Locate every blood parasite and identify its species.
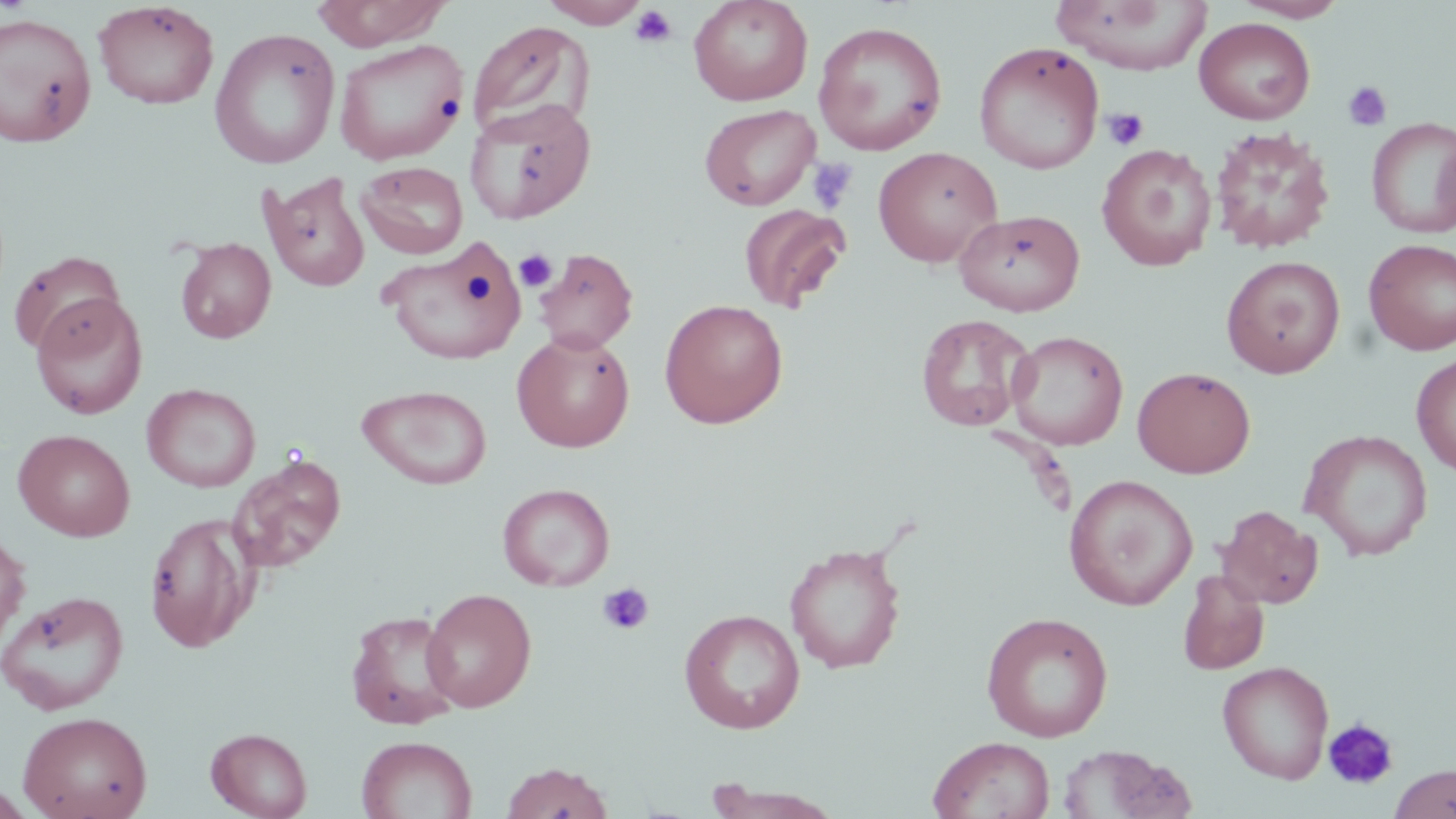
No blood parasites seen.

{
  "slide_level_diagnosis": "no evidence of blood parasites",
  "uninfected_red_blood_cell_locations": "approximate bounding boxes as named x1/y1/x2/y2 corners in pixels: (x1=311, y1=0, x2=452, y2=50), (x1=538, y1=0, x2=649, y2=27), (x1=688, y1=0, x2=814, y2=106), (x1=1050, y1=0, x2=1212, y2=74), (x1=1231, y1=0, x2=1350, y2=22), (x1=93, y1=1, x2=219, y2=110), (x1=0, y1=10, x2=206, y2=136), (x1=0, y1=11, x2=97, y2=147), (x1=1194, y1=17, x2=1315, y2=124), (x1=467, y1=20, x2=596, y2=138), (x1=813, y1=20, x2=948, y2=156), (x1=209, y1=27, x2=341, y2=169), (x1=334, y1=39, x2=468, y2=165), (x1=973, y1=41, x2=1104, y2=175), (x1=465, y1=100, x2=596, y2=225), (x1=699, y1=103, x2=820, y2=210), (x1=1366, y1=117, x2=1456, y2=238), (x1=1210, y1=126, x2=1335, y2=255), (x1=1096, y1=144, x2=1217, y2=271), (x1=873, y1=147, x2=1003, y2=268), (x1=356, y1=161, x2=468, y2=259), (x1=259, y1=172, x2=371, y2=292), (x1=739, y1=204, x2=850, y2=313), (x1=954, y1=208, x2=1085, y2=316), (x1=175, y1=237, x2=276, y2=343), (x1=380, y1=239, x2=528, y2=365), (x1=1363, y1=239, x2=1456, y2=355), (x1=534, y1=247, x2=639, y2=354), (x1=9, y1=250, x2=126, y2=356), (x1=1221, y1=255, x2=1345, y2=379), (x1=29, y1=294, x2=148, y2=419), (x1=659, y1=298, x2=788, y2=428), (x1=916, y1=313, x2=1035, y2=432), (x1=512, y1=331, x2=635, y2=452), (x1=1007, y1=331, x2=1128, y2=450), (x1=1411, y1=354, x2=1456, y2=477), (x1=1133, y1=366, x2=1256, y2=478), (x1=141, y1=383, x2=261, y2=492), (x1=356, y1=384, x2=493, y2=490), (x1=14, y1=429, x2=135, y2=542), (x1=1299, y1=429, x2=1433, y2=561), (x1=229, y1=452, x2=347, y2=574), (x1=1064, y1=474, x2=1197, y2=610), (x1=497, y1=483, x2=615, y2=591), (x1=1216, y1=505, x2=1323, y2=609), (x1=145, y1=514, x2=256, y2=654), (x1=0, y1=527, x2=29, y2=651), (x1=784, y1=541, x2=907, y2=674), (x1=1177, y1=570, x2=1270, y2=675), (x1=421, y1=588, x2=537, y2=712), (x1=0, y1=590, x2=130, y2=715), (x1=679, y1=608, x2=806, y2=735), (x1=345, y1=609, x2=461, y2=729), (x1=981, y1=611, x2=1113, y2=742), (x1=1217, y1=661, x2=1335, y2=784), (x1=18, y1=710, x2=152, y2=819), (x1=206, y1=727, x2=312, y2=818), (x1=928, y1=735, x2=1055, y2=819), (x1=356, y1=736, x2=477, y2=819), (x1=1056, y1=744, x2=1187, y2=818), (x1=500, y1=760, x2=614, y2=818), (x1=1389, y1=764, x2=1455, y2=819), (x1=703, y1=784, x2=845, y2=818)",
  "modality": "light microscopy",
  "field_of_view": "one of a larger specimen",
  "preparation": "thin blood smear",
  "image_size": "1456×819 pixels",
  "stain": "May-Grünwald-Giemsa",
  "platelet_locations": "approximate bounding boxes as named x1/y1/x2/y2 corners in pixels: (x1=630, y1=6, x2=678, y2=48), (x1=1343, y1=80, x2=1392, y2=132), (x1=1102, y1=108, x2=1149, y2=151), (x1=807, y1=157, x2=856, y2=213), (x1=514, y1=249, x2=557, y2=292), (x1=596, y1=582, x2=655, y2=635), (x1=1323, y1=718, x2=1399, y2=790)",
  "magnification": "1000x"
}